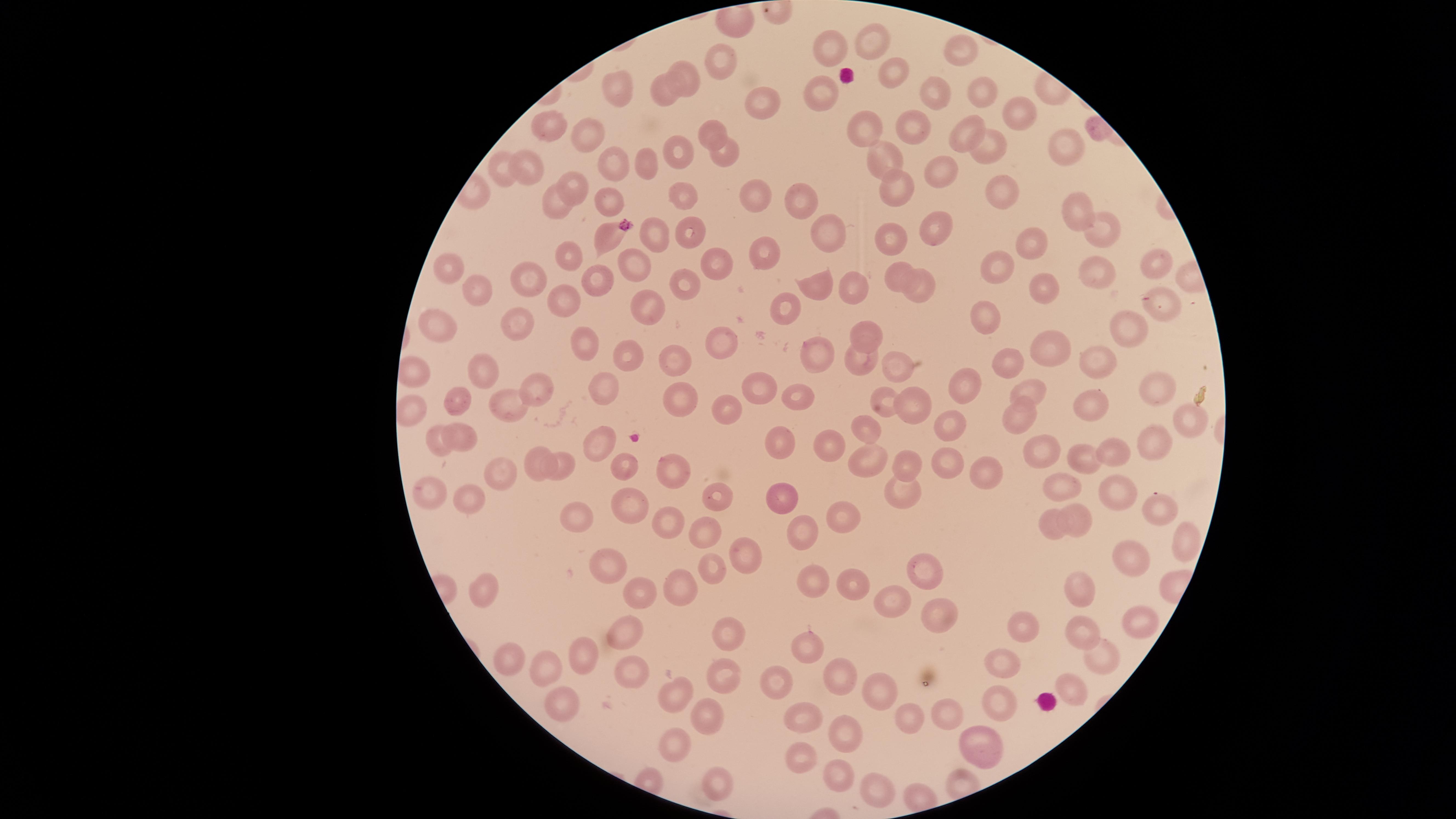
capture: smartphone photograph through the microscope eyepiece
stain: Giemsa
visible_region: circular
preparation: thin blood smear
presence: no malaria parasites identified
image_size: 1456×819 pixels
field_of_view: single
uninfected_red_blood_cells: 'approximate marker points as [x, y] in pixels: [875, 41], [837, 45], [955, 51], [724, 56], [892, 72], [681, 75], [618, 87], [660, 88], [818, 88], [980, 90], [933, 92], [760, 102], [1020, 113], [862, 123], [543, 126], [912, 127], [715, 130], [967, 132], [583, 135], [1064, 146], [988, 147], [673, 151], [728, 151], [884, 154], [642, 162], [613, 163], [941, 169], [500, 173], [533, 173], [897, 184], [999, 186], [578, 187], [678, 193], [757, 196], [613, 198], [799, 199], [553, 201], [1078, 206], [936, 223], [1107, 225], [827, 230], [607, 234], [897, 235], [658, 237], [689, 237], [1028, 240], [569, 250], [764, 250], [628, 259], [440, 262], [1154, 262], [718, 264], [997, 265], [901, 269], [529, 272], [1098, 273], [818, 282], [1040, 284], [592, 288], [685, 288], [848, 289], [921, 289], [559, 295], [475, 296], [1162, 306], [649, 308], [779, 311], [988, 316], [517, 320], [866, 326], [1126, 330], [437, 331], [577, 343], [1054, 345], [718, 346], [629, 349], [816, 350], [858, 355], [1007, 359], [1102, 359], [669, 361], [899, 365], [486, 370], [420, 372], [544, 379], [960, 379], [1154, 379], [602, 380], [754, 389], [1028, 391], [794, 395], [453, 399], [676, 400], [1092, 401], [511, 404], [725, 405], [886, 407], [1018, 410], [413, 411], [1188, 415], [953, 422], [866, 424], [469, 440], [605, 440], [781, 440], [1157, 441], [442, 443], [830, 446], [1044, 446], [1117, 451], [1083, 455], [947, 459], [906, 460], [621, 461], [872, 462], [565, 463], [536, 466], [674, 468], [505, 472], [996, 479], [1063, 485], [713, 487], [431, 489], [1115, 489], [906, 492], [632, 496], [781, 496], [464, 500], [1162, 501], [1074, 510], [843, 512], [580, 518], [674, 520], [1051, 526], [797, 528], [703, 531], [1186, 538], [746, 553], [1141, 561], [616, 567], [717, 569], [927, 576], [851, 580], [820, 583], [1075, 584], [487, 589], [639, 593], [682, 593], [941, 603], [895, 604], [1139, 619], [1075, 626], [729, 627], [1025, 630], [630, 631], [810, 642], [594, 653], [517, 658], [1100, 659], [1005, 660], [544, 668], [839, 672], [640, 674], [727, 675], [776, 686], [1074, 690], [878, 695], [680, 696], [996, 700], [563, 705], [703, 713], [801, 715], [950, 715], [910, 717], [841, 727], [676, 744], [984, 745], [805, 762], [831, 774], [718, 783], [874, 785]'